Locate and identify every blood parasite.
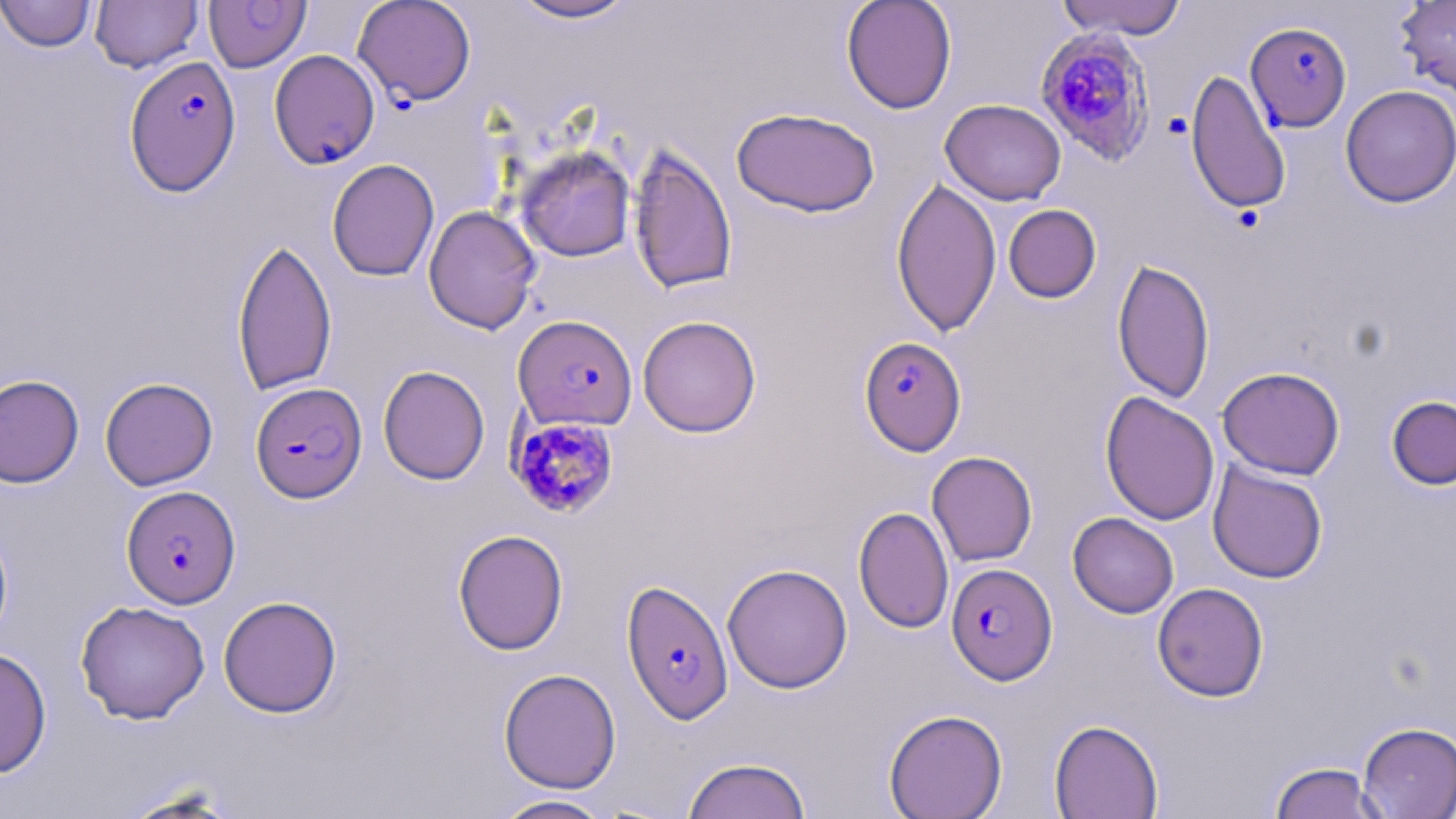
Approximate bounding boxes as (x1, y1, x2, y2) in pixels.
Plasmodium falciparum-infected red blood cells: (353, 0, 476, 106), (1243, 23, 1352, 132), (1034, 26, 1157, 168), (269, 49, 380, 169), (124, 56, 242, 196), (514, 314, 638, 430), (858, 334, 965, 462), (250, 382, 367, 501), (507, 416, 620, 518), (121, 486, 240, 608), (946, 562, 1058, 685), (621, 579, 734, 725).
No Plasmodium ovale, Plasmodium malariae, Plasmodium vivax, Babesia divergens, or Trypanosoma brucei observed.

Summary:
  - Uninfected red blood cell locations: (0, 0, 97, 53), (90, 0, 204, 73), (505, 0, 641, 25), (841, 0, 957, 114), (1055, 0, 1187, 40), (1395, 0, 1456, 98), (204, 1, 311, 72), (1185, 69, 1291, 214), (1340, 85, 1456, 207), (940, 99, 1066, 205), (731, 106, 880, 217), (628, 144, 737, 295), (515, 145, 636, 262), (327, 159, 440, 281), (891, 177, 1002, 338), (1003, 204, 1101, 303), (423, 205, 542, 334), (231, 237, 338, 396), (1112, 258, 1215, 404), (637, 315, 762, 437), (378, 365, 490, 485), (1217, 366, 1345, 480), (0, 374, 84, 488), (100, 377, 218, 491), (1100, 391, 1220, 526), (1386, 395, 1456, 490), (927, 451, 1038, 566), (1208, 461, 1328, 583), (853, 506, 954, 633), (1068, 512, 1179, 618), (0, 517, 14, 648), (452, 528, 569, 655), (722, 563, 853, 693), (1152, 582, 1269, 702), (218, 595, 343, 718), (75, 600, 210, 724), (0, 647, 52, 778), (498, 668, 622, 793), (884, 708, 1007, 819), (1048, 718, 1163, 819), (1357, 722, 1456, 818), (682, 756, 812, 819), (1269, 761, 1387, 819), (118, 787, 243, 818), (490, 795, 614, 818)
  - Slide-level diagnosis: Plasmodium falciparum
  - Field of view: one of a larger specimen
  - Magnification: 1000x
  - Stain: May-Grünwald-Giemsa
  - Image size: 1456×819 pixels
  - Modality: optical microscopy
  - Preparation: thin blood film